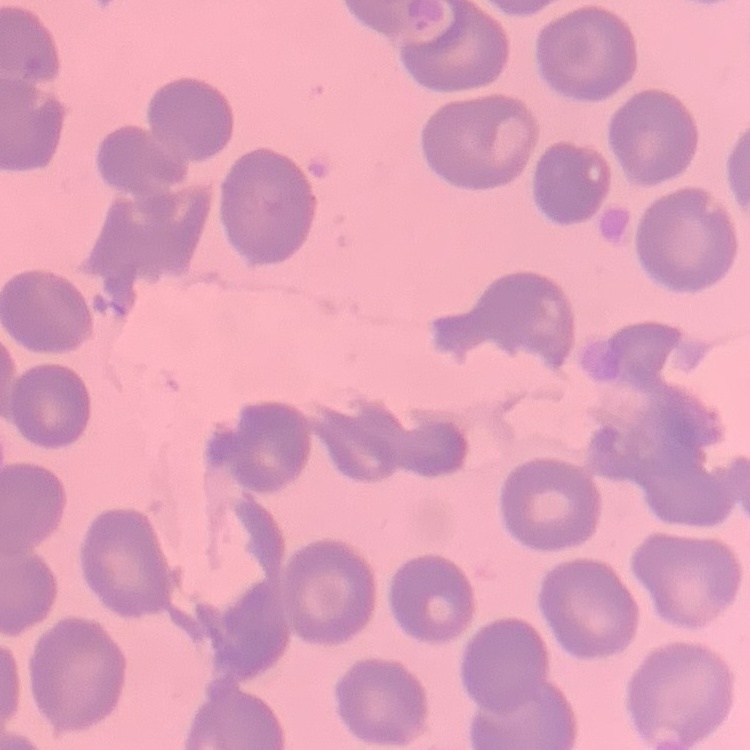

erythrocyte morphology = no rouleaux formation
stain = Field's or Giemsa
image type = one tile cut from a larger photomicrograph
preparation = thin blood film